Comment on the morphology of the erythrocytes.
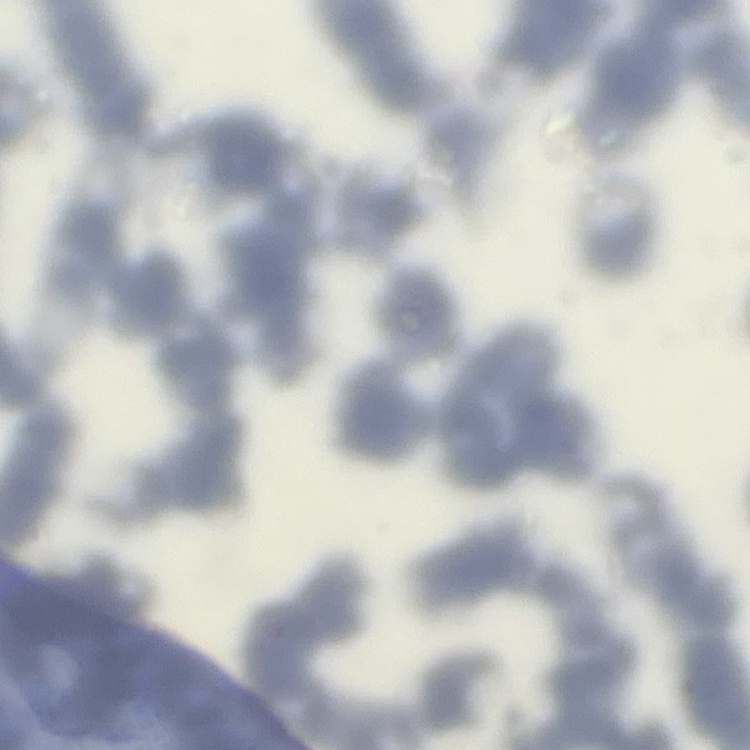

They show rouleaux formation.

{
  "image_type": "one tile cut from a larger photomicrograph",
  "preparation": "thin blood film",
  "stain": "Field's or Giemsa"
}